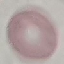 Malaria status: uninfected. Cell patch, automatically extracted from a larger field of view and resized to 64 × 64 pixels. Giemsa stain. Acquired by smartphone through the microscope eyepiece. Thin blood smear.